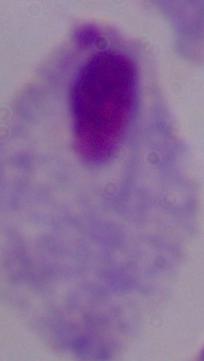
Micrograph. Captured at 1000x magnification. A trichomonad is shown.